Give the extent of all Plasmodium malariae-infected red blood cells.
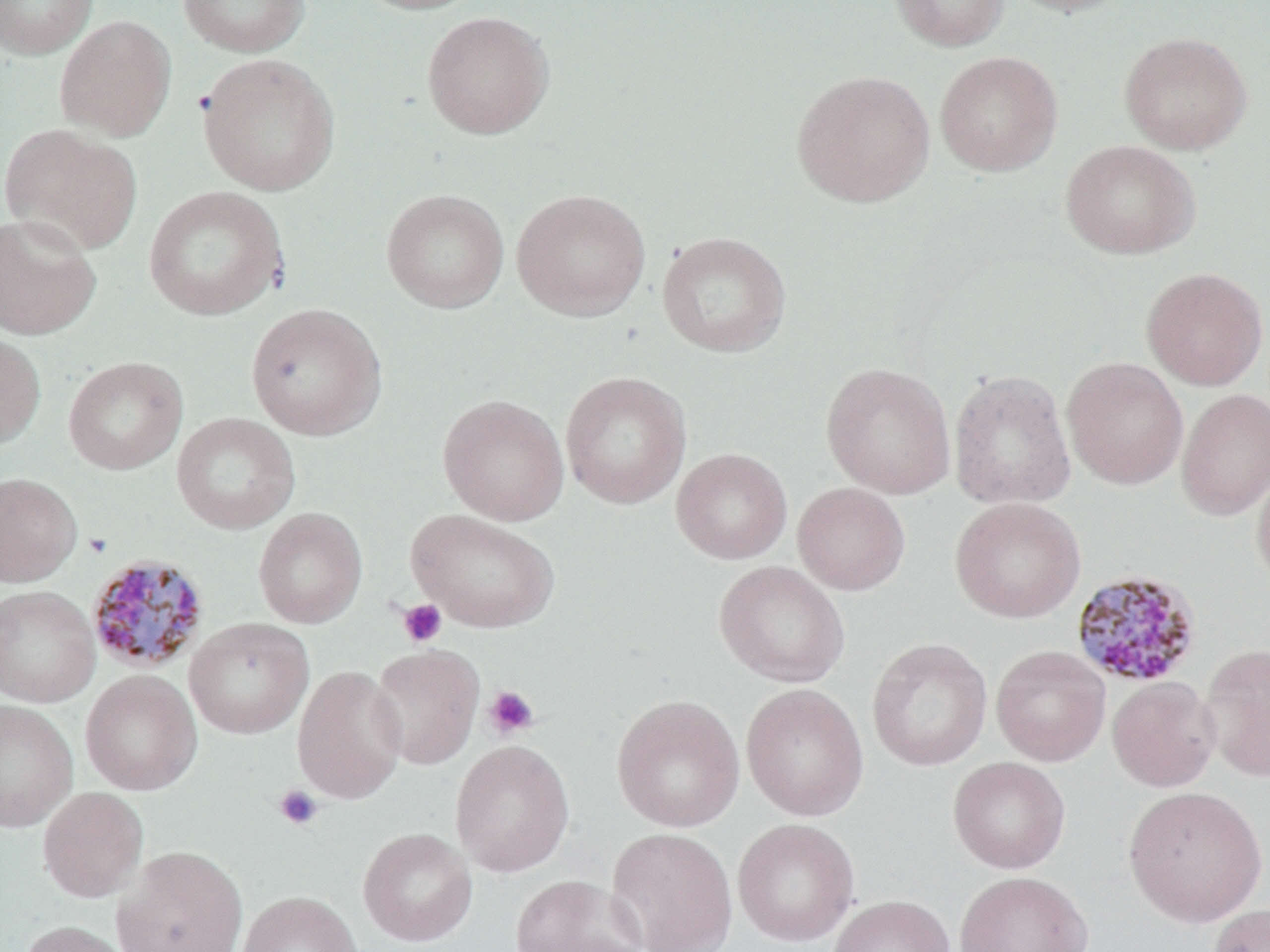

Approximate bounding boxes as named x1/y1/x2/y2 corners in pixels.
Plasmodium malariae-infected red blood cells: (x1=85, y1=552, x2=210, y2=676), (x1=1070, y1=568, x2=1204, y2=689).

Uninfected red blood cell locations: (x1=0, y1=0, x2=98, y2=59), (x1=177, y1=0, x2=311, y2=58), (x1=350, y1=0, x2=489, y2=15), (x1=889, y1=0, x2=1010, y2=52), (x1=1002, y1=0, x2=1134, y2=17), (x1=421, y1=11, x2=554, y2=140), (x1=54, y1=15, x2=176, y2=141), (x1=1119, y1=31, x2=1253, y2=155), (x1=934, y1=51, x2=1063, y2=176), (x1=197, y1=53, x2=340, y2=195), (x1=790, y1=70, x2=935, y2=207), (x1=1, y1=125, x2=143, y2=255), (x1=1060, y1=140, x2=1201, y2=259), (x1=143, y1=186, x2=288, y2=320), (x1=381, y1=188, x2=509, y2=313), (x1=511, y1=188, x2=651, y2=321), (x1=0, y1=212, x2=101, y2=340), (x1=657, y1=231, x2=792, y2=357), (x1=1141, y1=267, x2=1268, y2=390), (x1=245, y1=302, x2=387, y2=440), (x1=0, y1=329, x2=46, y2=451), (x1=63, y1=356, x2=188, y2=475), (x1=1061, y1=357, x2=1189, y2=489), (x1=821, y1=363, x2=956, y2=499), (x1=948, y1=369, x2=1076, y2=510), (x1=560, y1=371, x2=691, y2=509), (x1=1176, y1=388, x2=1270, y2=520), (x1=437, y1=394, x2=569, y2=526), (x1=172, y1=412, x2=300, y2=535), (x1=671, y1=448, x2=793, y2=565), (x1=1252, y1=461, x2=1270, y2=589), (x1=0, y1=472, x2=82, y2=587), (x1=792, y1=482, x2=910, y2=595), (x1=949, y1=497, x2=1086, y2=623), (x1=253, y1=507, x2=367, y2=629), (x1=406, y1=508, x2=560, y2=633), (x1=713, y1=560, x2=850, y2=688), (x1=0, y1=585, x2=100, y2=708), (x1=184, y1=617, x2=314, y2=739), (x1=866, y1=637, x2=992, y2=771), (x1=1199, y1=643, x2=1270, y2=782), (x1=368, y1=644, x2=485, y2=770), (x1=990, y1=645, x2=1110, y2=766), (x1=292, y1=665, x2=407, y2=804), (x1=80, y1=669, x2=202, y2=796), (x1=1107, y1=676, x2=1220, y2=792), (x1=741, y1=683, x2=869, y2=821), (x1=611, y1=694, x2=745, y2=832), (x1=0, y1=699, x2=78, y2=832), (x1=450, y1=739, x2=575, y2=877), (x1=948, y1=757, x2=1070, y2=873), (x1=1122, y1=785, x2=1268, y2=927), (x1=37, y1=786, x2=148, y2=903), (x1=732, y1=818, x2=860, y2=946), (x1=357, y1=827, x2=477, y2=947), (x1=606, y1=827, x2=738, y2=952), (x1=114, y1=846, x2=249, y2=952), (x1=954, y1=871, x2=1094, y2=952), (x1=510, y1=874, x2=648, y2=952), (x1=237, y1=890, x2=362, y2=952), (x1=827, y1=894, x2=955, y2=952), (x1=1207, y1=902, x2=1270, y2=952), (x1=18, y1=920, x2=135, y2=952). Platelet locations: (x1=83, y1=532, x2=112, y2=558), (x1=397, y1=599, x2=447, y2=647), (x1=482, y1=685, x2=541, y2=740), (x1=273, y1=785, x2=324, y2=831). Slide-level diagnosis: Plasmodium malariae. One field of a larger specimen. May-Grünwald-Giemsa-stained preparation. Optical microscopy. Image is 1270×952 pixels. Thin blood smear. 1000x magnification.